Assess this cell for malaria.
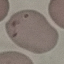

Uninfected.

Giemsa-stained preparation. Cell patch, automatically extracted from a larger field of view and resized to 64 × 64 pixels. Thin smear of blood. Photographed with a smartphone camera at the microscope eyepiece.